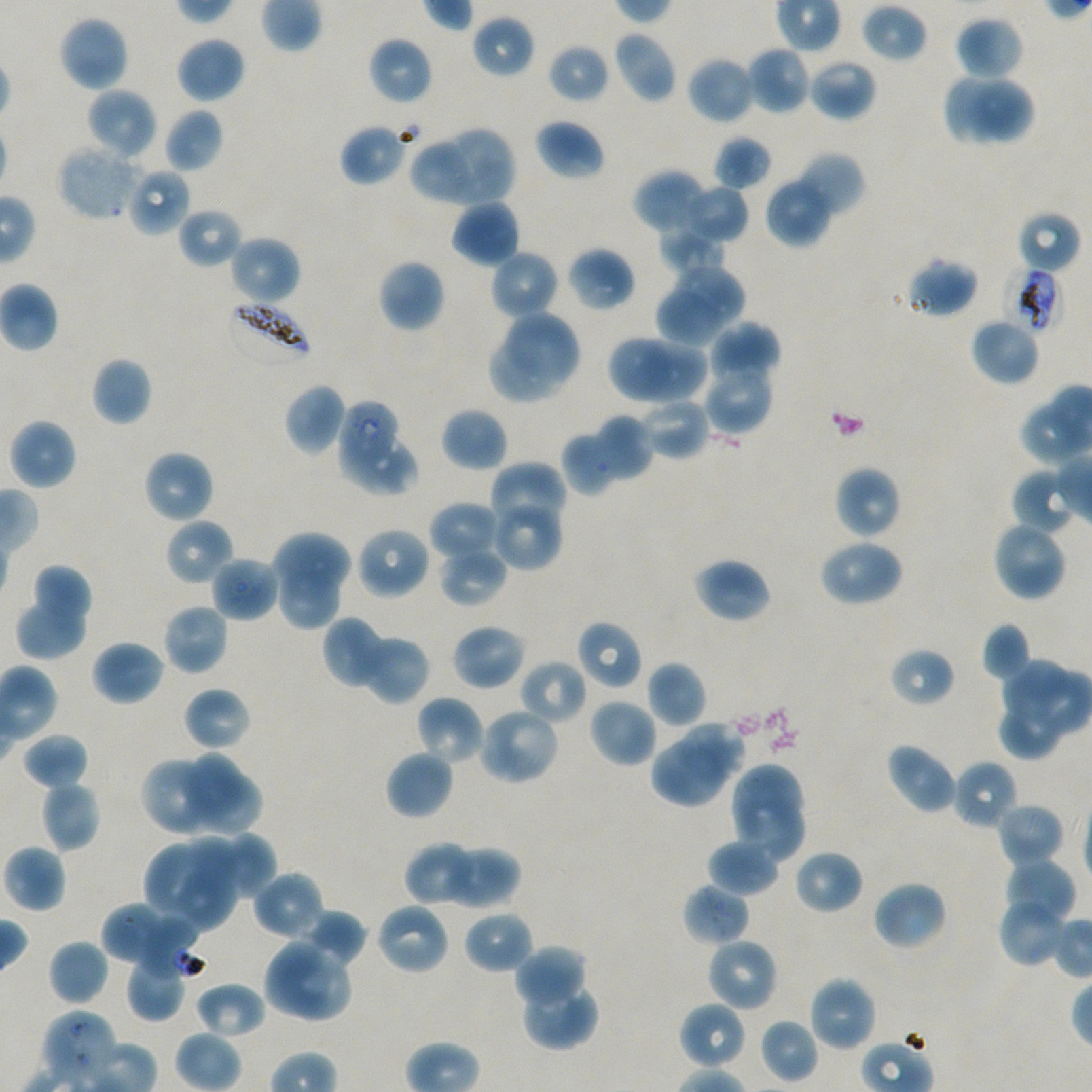 Approximate bounding boxes as (x1, y1, x2, y2) in pixels. Not every red blood cell is marked. Locations of uninfected red blood cells: (861, 3, 927, 63), (471, 14, 534, 79), (57, 15, 130, 92), (954, 16, 1023, 81), (612, 31, 678, 104), (175, 36, 246, 104), (368, 37, 433, 105), (548, 43, 611, 104), (745, 45, 811, 115), (686, 55, 757, 125), (808, 59, 877, 121), (941, 72, 1008, 146), (971, 79, 1036, 143), (86, 87, 158, 160), (164, 108, 223, 173), (534, 118, 605, 181), (339, 124, 407, 186), (440, 128, 515, 204), (714, 135, 772, 191), (408, 142, 473, 206), (56, 143, 143, 221), (793, 152, 865, 219), (126, 167, 191, 237), (632, 168, 708, 234), (765, 175, 834, 248), (679, 183, 748, 247), (450, 198, 521, 269), (177, 207, 244, 268), (1015, 210, 1081, 274), (658, 228, 727, 275), (228, 234, 301, 306), (566, 246, 636, 312), (489, 249, 559, 320), (903, 258, 978, 318), (378, 259, 446, 333), (674, 263, 748, 329), (655, 290, 725, 347), (506, 310, 581, 382), (970, 316, 1040, 386), (708, 322, 780, 385), (608, 333, 672, 404), (608, 333, 708, 405), (489, 340, 565, 404), (641, 344, 710, 405), (91, 357, 152, 426), (704, 361, 773, 434), (283, 382, 347, 455), (637, 397, 710, 461), (441, 407, 509, 472), (593, 414, 654, 479), (8, 418, 77, 490), (562, 432, 617, 495), (342, 435, 421, 498), (143, 450, 214, 524), (490, 462, 565, 533), (833, 466, 901, 539), (1014, 472, 1077, 531), (490, 496, 562, 571), (429, 500, 503, 562), (165, 517, 234, 587), (992, 520, 1068, 602), (356, 526, 430, 600), (270, 531, 353, 598), (818, 539, 905, 607), (439, 545, 507, 606), (210, 555, 279, 623), (692, 558, 771, 624), (31, 564, 98, 620), (278, 569, 341, 632), (14, 598, 86, 659), (162, 603, 229, 676), (322, 616, 393, 690), (576, 620, 642, 690), (451, 623, 527, 691), (981, 623, 1032, 682), (357, 634, 430, 704), (91, 639, 165, 706), (888, 647, 956, 708), (520, 659, 587, 726), (1001, 659, 1070, 721), (646, 661, 706, 729), (1032, 672, 1090, 735), (183, 687, 251, 751), (415, 696, 486, 766), (589, 698, 658, 768), (476, 706, 560, 786), (996, 706, 1059, 760), (676, 721, 748, 780), (21, 732, 89, 790), (651, 741, 729, 809), (884, 742, 958, 815), (385, 750, 454, 820), (185, 752, 248, 817), (141, 757, 213, 835), (951, 759, 1019, 831), (729, 763, 805, 826), (204, 774, 264, 837), (39, 780, 101, 852), (734, 797, 805, 864), (997, 806, 1061, 865), (224, 831, 276, 898), (183, 836, 240, 894), (706, 838, 780, 896), (404, 841, 484, 907), (2, 843, 66, 913), (142, 844, 209, 911), (441, 844, 520, 909), (793, 850, 863, 915), (1008, 852, 1077, 928), (175, 867, 236, 932), (252, 869, 325, 941), (873, 879, 947, 951), (1001, 900, 1063, 967), (374, 901, 450, 976), (102, 903, 169, 963), (302, 909, 367, 966), (462, 909, 533, 974), (706, 937, 778, 1013), (48, 939, 109, 1006), (263, 939, 334, 1018), (513, 944, 586, 1011), (124, 956, 187, 1022), (291, 956, 352, 1022), (520, 975, 598, 1051), (807, 975, 879, 1052), (194, 981, 268, 1040), (678, 1000, 747, 1070), (760, 1018, 819, 1083). Locations of red blood cells of indeterminate infection status: (1004, 266, 1063, 334), (337, 400, 397, 469), (682, 884, 750, 946), (137, 921, 206, 980), (41, 1011, 118, 1085). Locations of infected red blood cells: (225, 297, 313, 368). Giemsa-stained preparation. Plasmodium falciparum strain NF54 maintained in static in-vitro culture. Thin blood film. One field from this slide. Image is 1092×1092 pixels. 100x objective under oil immersion, numerical aperture 1.45. Blood group of the donor: A+/O+.